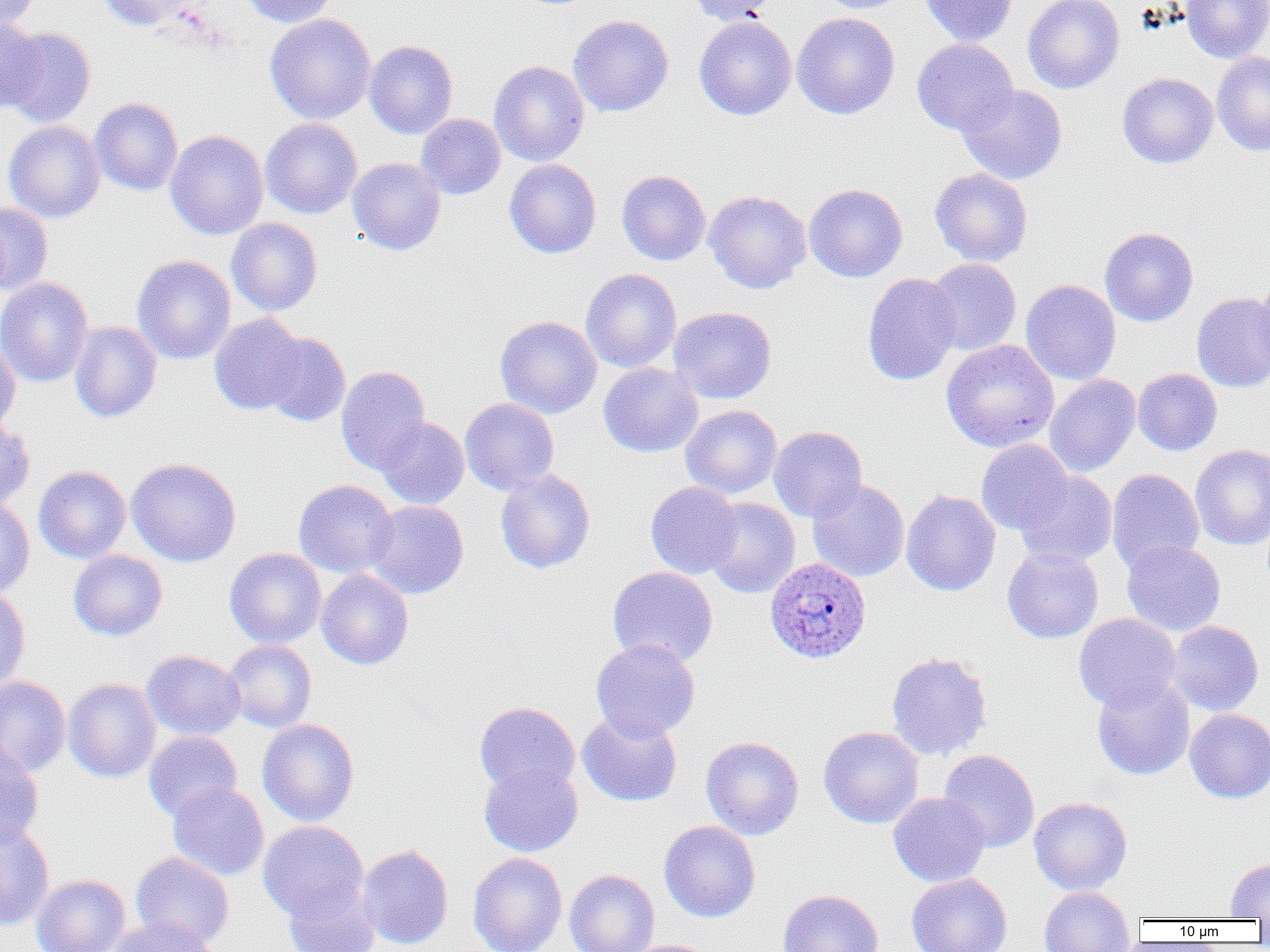
Approximate bounding boxes as (x1, y1, x2, y2) in pixels. Uninfected red blood cell locations: (0, 0, 41, 30), (97, 0, 195, 31), (240, 0, 338, 27), (687, 0, 784, 25), (814, 0, 911, 14), (920, 0, 1018, 47), (1023, 0, 1124, 94), (1180, 0, 1270, 63), (791, 12, 900, 120), (264, 14, 376, 125), (567, 15, 674, 117), (693, 15, 797, 120), (0, 18, 46, 113), (3, 27, 96, 127), (911, 38, 1018, 136), (364, 40, 458, 139), (1211, 50, 1270, 156), (488, 60, 590, 167), (1117, 72, 1219, 168), (957, 83, 1067, 185), (89, 97, 183, 196), (416, 114, 505, 200), (260, 117, 362, 219), (4, 121, 105, 222), (164, 130, 268, 240), (347, 157, 446, 255), (504, 159, 601, 259), (930, 168, 1033, 266), (617, 170, 710, 266), (804, 183, 907, 282), (703, 190, 811, 294), (0, 201, 53, 295), (226, 218, 323, 316), (1099, 226, 1199, 327), (132, 255, 236, 364), (925, 258, 1022, 356), (580, 268, 682, 373), (862, 272, 962, 386), (1253, 274, 1270, 376), (0, 277, 93, 387), (1021, 279, 1121, 385), (1191, 293, 1270, 393), (668, 306, 777, 404), (209, 314, 308, 416), (495, 315, 602, 418), (69, 321, 162, 423), (260, 332, 350, 426), (0, 338, 21, 435), (941, 339, 1059, 453), (598, 362, 703, 458), (335, 365, 431, 475), (1132, 368, 1222, 456), (1044, 374, 1141, 477), (459, 398, 559, 495), (681, 405, 782, 499), (376, 416, 469, 509), (0, 418, 35, 512), (768, 425, 867, 523), (975, 439, 1073, 535), (1190, 443, 1270, 550), (125, 457, 242, 567), (33, 465, 131, 563), (495, 469, 595, 573), (1106, 469, 1204, 574), (1014, 470, 1118, 568), (806, 478, 909, 582), (293, 479, 399, 579), (645, 481, 742, 579), (901, 489, 1001, 596), (0, 497, 35, 598), (703, 497, 800, 598), (365, 500, 469, 599), (1122, 540, 1226, 636), (1002, 547, 1103, 644), (225, 548, 327, 649), (68, 550, 168, 641), (607, 566, 718, 668), (316, 568, 414, 670), (0, 586, 31, 695), (1073, 613, 1182, 712), (1167, 620, 1264, 716), (590, 638, 700, 741), (223, 639, 316, 733), (141, 649, 246, 741), (886, 651, 993, 760), (0, 676, 72, 777), (1091, 676, 1194, 781), (63, 677, 161, 782), (473, 701, 580, 796), (1185, 709, 1270, 804), (577, 710, 682, 807), (257, 718, 359, 827), (818, 726, 924, 828), (143, 732, 241, 823), (701, 736, 804, 840), (0, 742, 44, 851), (938, 749, 1040, 852), (479, 762, 583, 857), (168, 782, 269, 881), (888, 792, 991, 888), (1028, 796, 1132, 895), (659, 820, 761, 922), (257, 821, 368, 921), (0, 822, 55, 931), (357, 845, 454, 949), (130, 851, 234, 950), (468, 852, 567, 952), (1225, 858, 1270, 919), (564, 869, 660, 952), (31, 873, 130, 952), (905, 873, 1012, 952), (282, 880, 380, 952), (1038, 885, 1136, 952), (776, 889, 883, 952), (104, 916, 221, 952), (625, 939, 722, 952). Plasmodium ovale-infected red blood cell locations: (764, 558, 871, 663). Slide-level diagnosis: Plasmodium ovale. Thin blood smear. Light microscopy. Captured at 1000x magnification. Single field of view. Image is 1270×952 pixels.